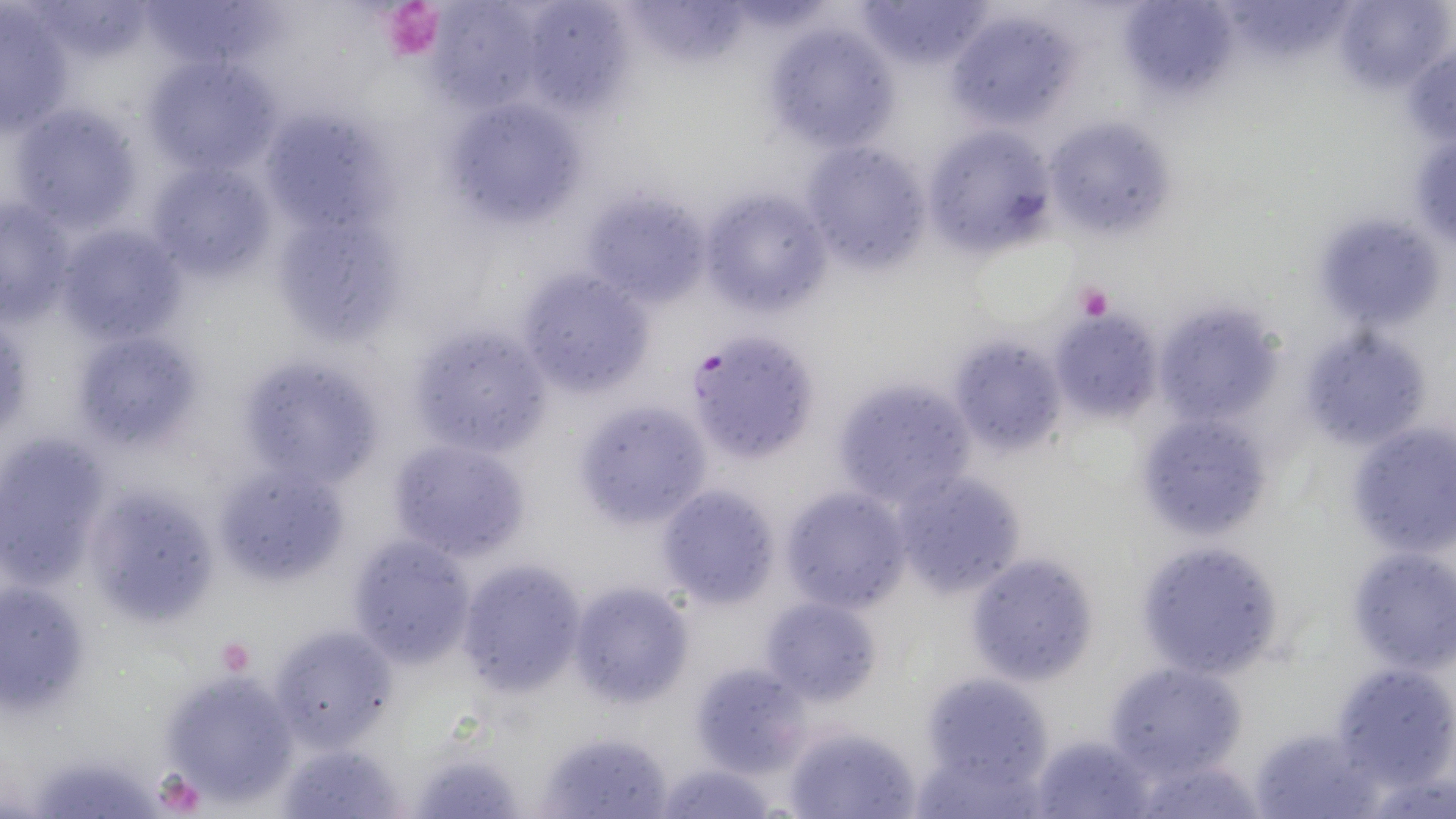

slide_level_diagnosis: Plasmodium falciparum
platelet_locations: 'approximate bounding boxes as [x1, y1, x2, y2] in pixels: [379, 2, 445, 60], [1077, 283, 1113, 321], [216, 637, 253, 675], [151, 772, 206, 813]'
preparation: thin blood film
modality: light microscopy
stain: May-Grünwald-Giemsa
field_of_view: one of a larger specimen
magnification: 1000x
uninfected_red_blood_cell_locations: 'approximate bounding boxes as [x1, y1, x2, y2] in pixels: [855, 0, 991, 72], [1224, 1, 1350, 62], [1336, 1, 1451, 94], [147, 2, 294, 74], [426, 2, 543, 111], [631, 2, 752, 64], [1125, 2, 1241, 100], [530, 4, 641, 114], [1, 5, 75, 135], [947, 10, 1076, 128], [762, 23, 895, 151], [1401, 49, 1456, 143], [141, 56, 284, 180], [439, 93, 589, 227], [9, 101, 146, 233], [1041, 116, 1175, 243], [267, 118, 402, 243], [922, 126, 1058, 257], [798, 142, 929, 272], [148, 164, 273, 277], [698, 187, 834, 317], [579, 189, 713, 304], [0, 198, 77, 324], [56, 220, 189, 345], [275, 220, 406, 349], [1329, 220, 1444, 334], [515, 269, 653, 394], [1152, 303, 1285, 431], [1048, 309, 1164, 422], [407, 321, 554, 458], [72, 326, 204, 455], [1301, 327, 1430, 450], [948, 336, 1070, 454], [235, 356, 385, 489], [830, 377, 975, 507], [572, 400, 712, 527], [1134, 414, 1274, 542], [1344, 423, 1455, 558], [0, 434, 107, 586], [386, 438, 531, 562], [216, 462, 350, 586], [890, 467, 1028, 598], [655, 484, 781, 608], [100, 485, 218, 617], [780, 487, 912, 613], [346, 536, 478, 665], [1134, 539, 1287, 679], [1346, 546, 1455, 672], [967, 553, 1099, 684], [455, 559, 588, 698], [0, 578, 93, 717], [569, 581, 691, 709], [759, 596, 882, 705], [268, 623, 397, 750], [1102, 660, 1248, 780], [691, 662, 809, 775], [1329, 662, 1455, 785], [163, 669, 302, 807], [918, 669, 1056, 801], [1249, 723, 1382, 819], [782, 725, 924, 818], [541, 729, 676, 819], [1028, 731, 1158, 819], [278, 741, 407, 818], [411, 743, 525, 819], [1130, 754, 1265, 819], [36, 756, 154, 819], [653, 759, 777, 819]'
image_size: 1456×819 pixels
plasmodium_falciparum_infected_red_blood_cell_locations: 'approximate bounding boxes as [x1, y1, x2, y2] in pixels: [686, 329, 820, 463]'